Report the malaria status of this cell.
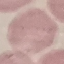

It is uninfected.

preparation = thin smear
stain = Giemsa
capture = smartphone camera at the microscope eyepiece
image type = cell patch, automatically extracted from a larger field of view and resized to 64 × 64 pixels